Give the preparation type.
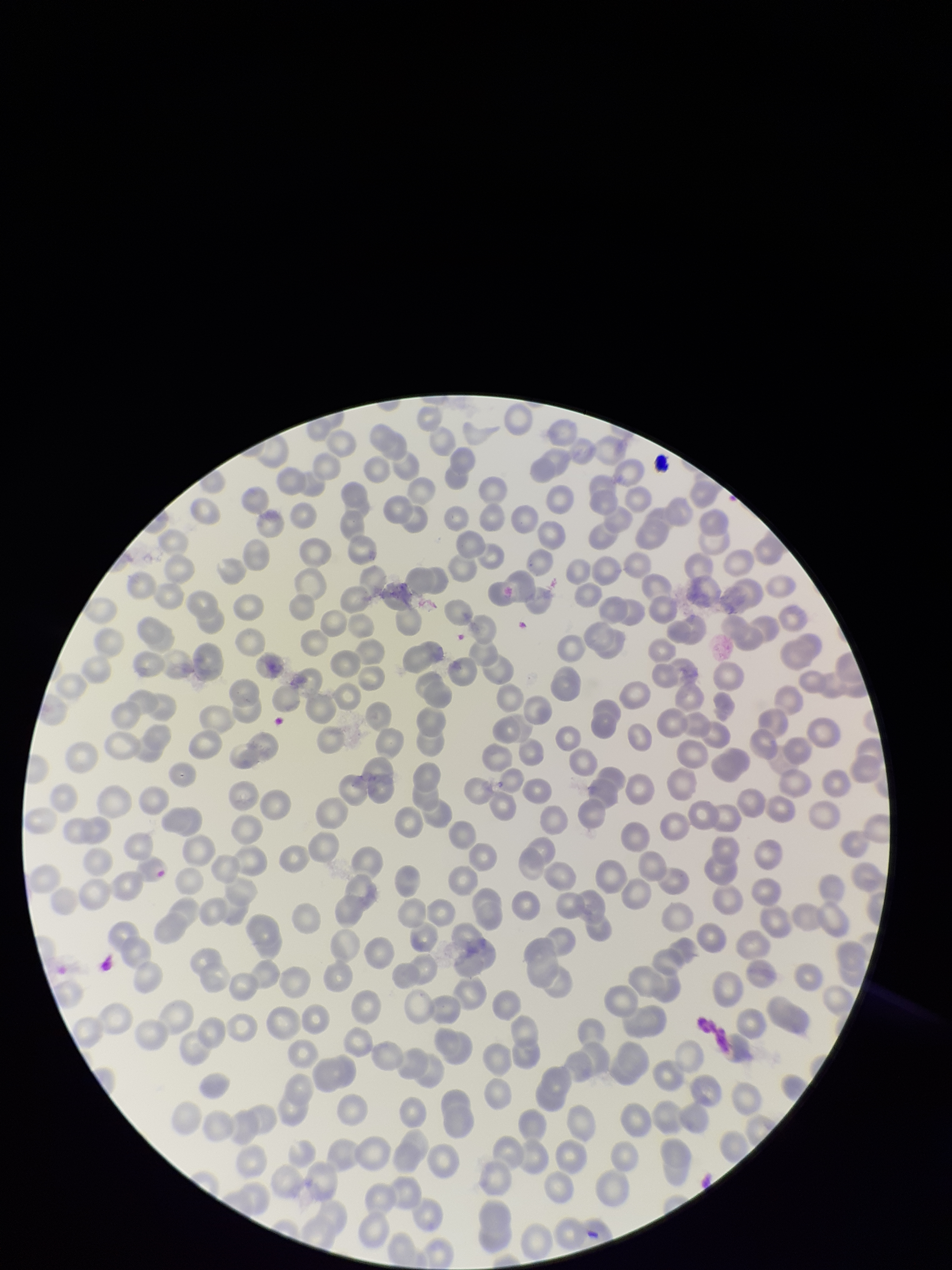

It is a thin blood smear.

Summary:
  - Field of view: single
  - Stain: Giemsa
  - Parasitized red blood cells: none seen
  - Parasitized red blood cell count: 0
  - Capture: smartphone photograph through the microscope eyepiece
  - Image size: 952×1270 pixels
  - Red blood cell count: 280
  - Patient malaria status: negative